Locate every malaria parasite and every leukocyte.
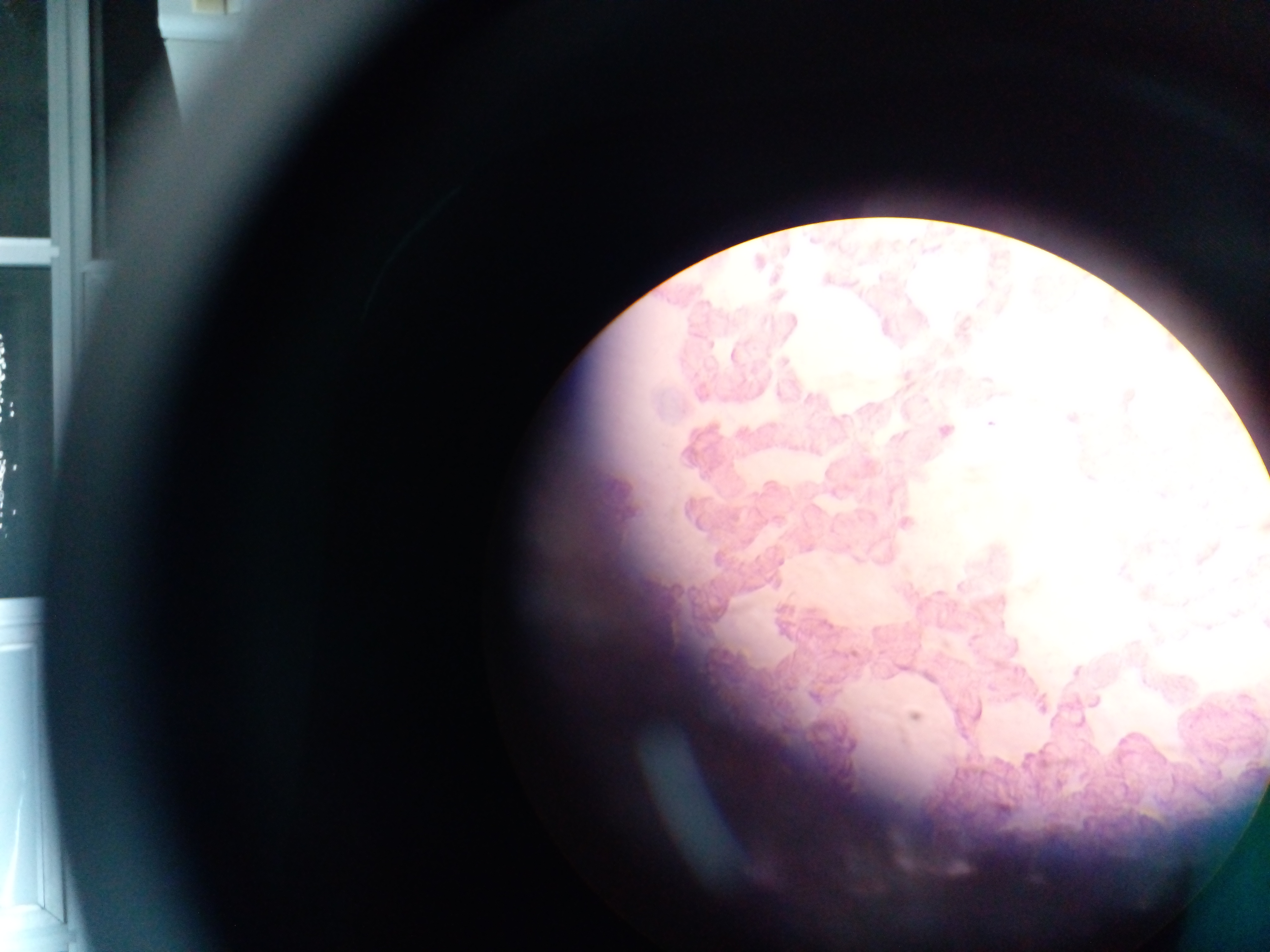

Approximate centers as [x, y] in pixels.
Malaria parasites: [979, 303], [987, 380], [1071, 417], [990, 423], [945, 431], [1090, 477], [1161, 495], [1204, 505], [1263, 528], [1146, 549], [1203, 558], [1260, 559], [780, 562], [1122, 572], [1234, 613], [1263, 623], [1208, 628], [900, 670], [1076, 671], [978, 712], [916, 716].
No leukocytes observed.

Summary:
  - Image size: 1270×952 pixels
  - Field of view: single
  - Preparation: thick blood film
  - Capture: mobile-phone photograph through a microscope
  - Country: Ghana